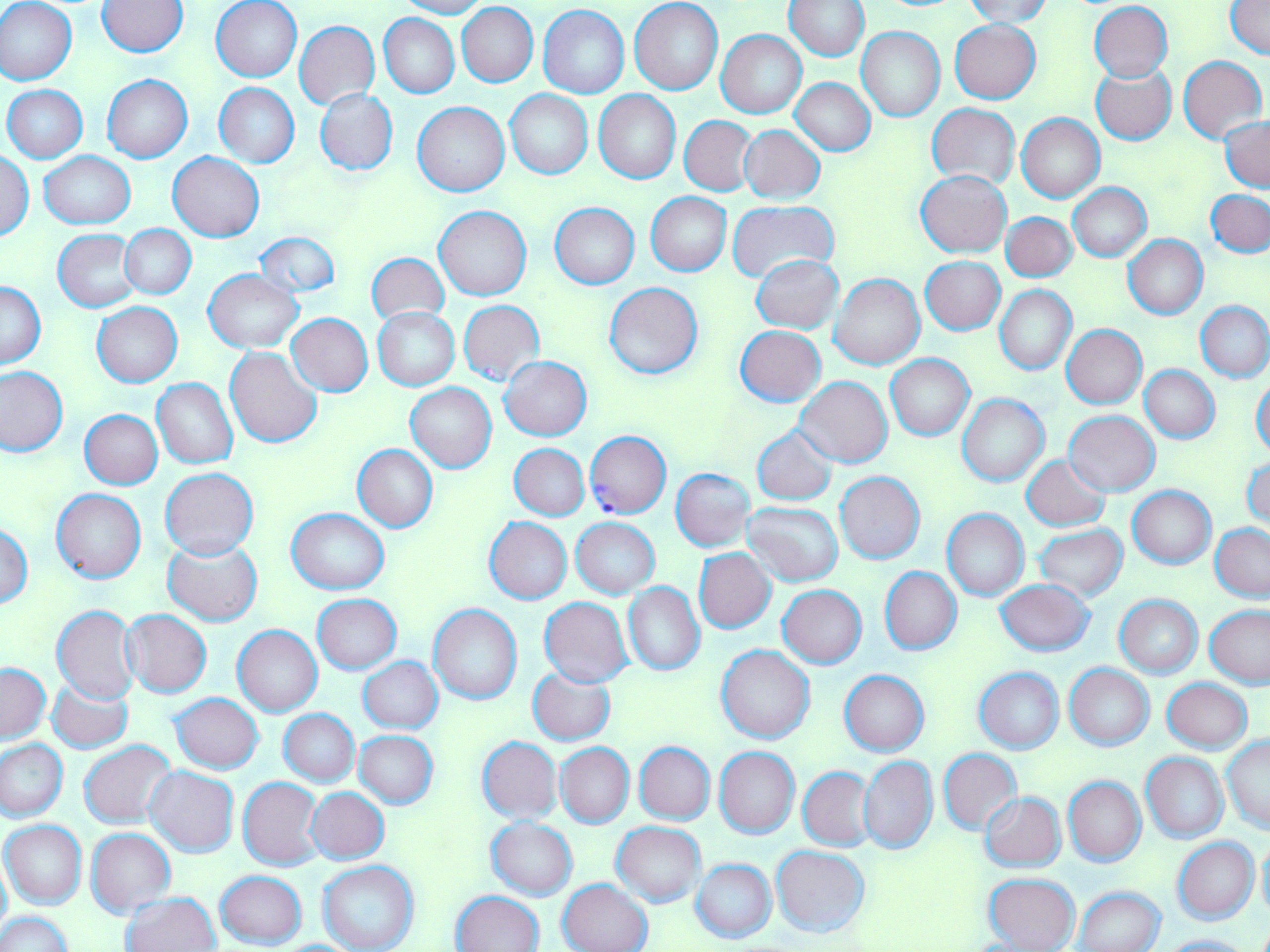 Approximate bounding boxes as (x1,y1)-(x2,y2) corner pairs in pixels. Uninfected red blood cell locations: (0,0)-(78,85), (394,0)-(487,18), (98,1)-(188,56), (212,1)-(302,81), (630,1)-(722,94), (785,1)-(869,60), (963,1)-(1055,26), (1088,2)-(1173,82), (1226,2)-(1270,60), (456,3)-(538,86), (538,6)-(630,98), (379,13)-(459,98), (949,20)-(1040,103), (294,21)-(379,108), (856,27)-(944,122), (716,29)-(807,119), (1177,55)-(1267,144), (1090,64)-(1176,145), (102,75)-(192,163), (791,78)-(875,156), (215,83)-(298,167), (3,85)-(87,162), (314,88)-(398,176), (505,89)-(593,179), (594,90)-(681,184), (413,102)-(509,196), (928,103)-(1018,190), (1017,114)-(1104,202), (679,116)-(757,195), (1221,117)-(1269,191), (739,124)-(825,203), (1,151)-(34,240), (39,151)-(135,228), (168,152)-(264,241), (917,170)-(1010,256), (1069,183)-(1151,260), (1206,188)-(1269,258), (645,192)-(731,276), (729,202)-(839,283), (549,203)-(639,289), (434,206)-(531,300), (1001,213)-(1077,281), (120,224)-(196,299), (53,230)-(141,311), (254,232)-(340,297), (1122,235)-(1208,319), (366,252)-(449,324), (752,254)-(843,333), (920,256)-(1005,335), (203,269)-(304,353), (831,274)-(924,370), (0,280)-(45,368), (604,282)-(703,380), (994,285)-(1077,375), (457,301)-(545,386), (1195,301)-(1270,383), (92,303)-(181,386), (374,308)-(459,389), (286,313)-(373,396), (1062,324)-(1147,408), (735,325)-(826,406), (225,346)-(322,448), (886,354)-(974,440), (500,356)-(591,441), (0,365)-(68,455), (1141,366)-(1220,443), (794,376)-(892,468), (1251,376)-(1270,458), (152,378)-(237,468), (405,383)-(496,473), (958,394)-(1049,487), (79,409)-(162,489), (1064,411)-(1159,497), (751,426)-(838,505), (509,443)-(589,520), (352,444)-(437,532), (1021,454)-(1111,531), (1243,455)-(1269,534), (161,468)-(258,559), (671,468)-(754,550), (835,471)-(925,564), (1128,486)-(1215,569), (52,489)-(145,584), (741,500)-(843,586), (286,508)-(390,594), (941,509)-(1029,601), (484,517)-(572,603), (571,517)-(659,598), (0,522)-(34,607), (1210,523)-(1270,601), (1034,524)-(1127,601), (164,539)-(262,626), (694,549)-(776,633), (880,566)-(961,655), (995,578)-(1094,657), (623,582)-(704,676), (777,585)-(867,669), (312,593)-(401,673), (1115,594)-(1202,678), (539,597)-(633,687), (429,604)-(521,704), (1205,604)-(1270,688), (52,605)-(139,703), (120,610)-(212,697), (232,625)-(322,717), (716,644)-(815,744), (358,657)-(443,733), (1,664)-(49,744), (1064,664)-(1154,750), (528,666)-(616,745), (974,668)-(1063,753), (840,670)-(929,757), (46,678)-(133,754), (1162,678)-(1252,753), (170,693)-(264,774), (280,709)-(358,787), (354,731)-(439,809), (478,736)-(561,823), (1221,736)-(1270,832), (1,739)-(67,821), (79,740)-(177,829), (635,742)-(715,824), (556,743)-(634,827), (715,747)-(799,839), (938,749)-(1022,834), (1141,752)-(1228,843), (859,756)-(937,854), (144,766)-(238,857), (798,767)-(875,851), (239,777)-(323,870), (1063,777)-(1145,866), (305,787)-(389,864), (979,791)-(1065,871), (486,816)-(577,899), (2,820)-(86,910), (612,822)-(706,907), (85,829)-(175,917), (1173,837)-(1259,924), (1256,838)-(1270,922), (566,846)-(695,943), (771,846)-(870,937), (0,854)-(11,943), (691,859)-(776,942), (318,860)-(419,952), (214,870)-(306,949), (983,873)-(1080,952), (559,878)-(652,952), (1074,886)-(1165,952), (453,891)-(544,952), (121,892)-(221,952), (1,912)-(73,952), (1162,934)-(1252,952). Plasmodium falciparum-infected red blood cell locations: (584,431)-(670,519). Slide-level diagnosis: Plasmodium falciparum. Thin blood film. Image is 1270×952 pixels. May-Grünwald-Giemsa-stained preparation. Light microscopy. One field of a larger specimen. Captured at 1000x magnification.